Describe the morphology of the erythrocytes.
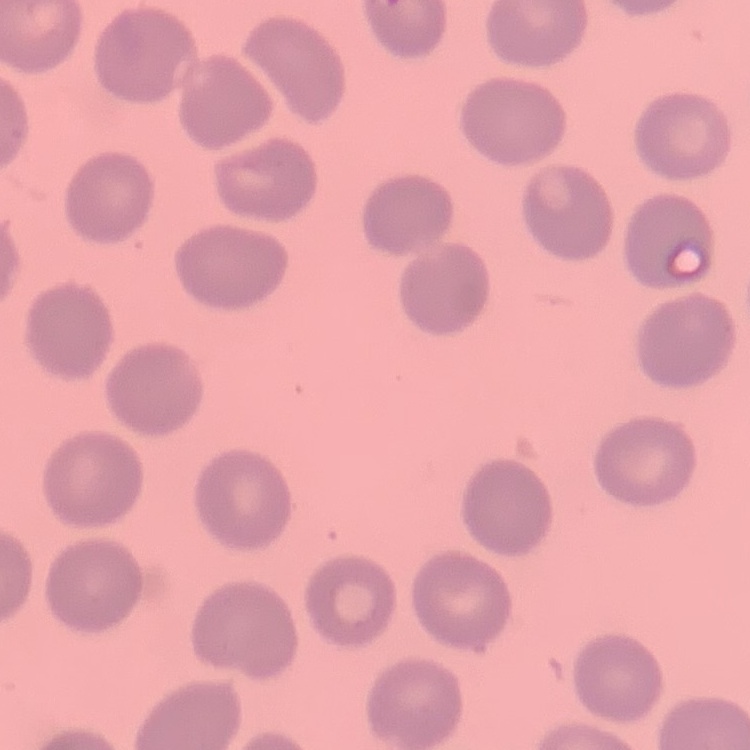
No rouleaux formation.

image type = square crop of a larger photomicrograph
preparation = thin peripheral smear
stain = Field's or Giemsa